Name the cell type shown.
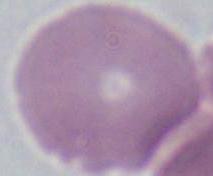

An erythrocyte.

1000x magnification. Photomicrograph.